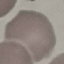
malaria status = uninfected
image type = automatically extracted cell patch, resized to 64 × 64 pixels
stain = Giemsa
capture = smartphone through the microscope eyepiece
preparation = thin smear